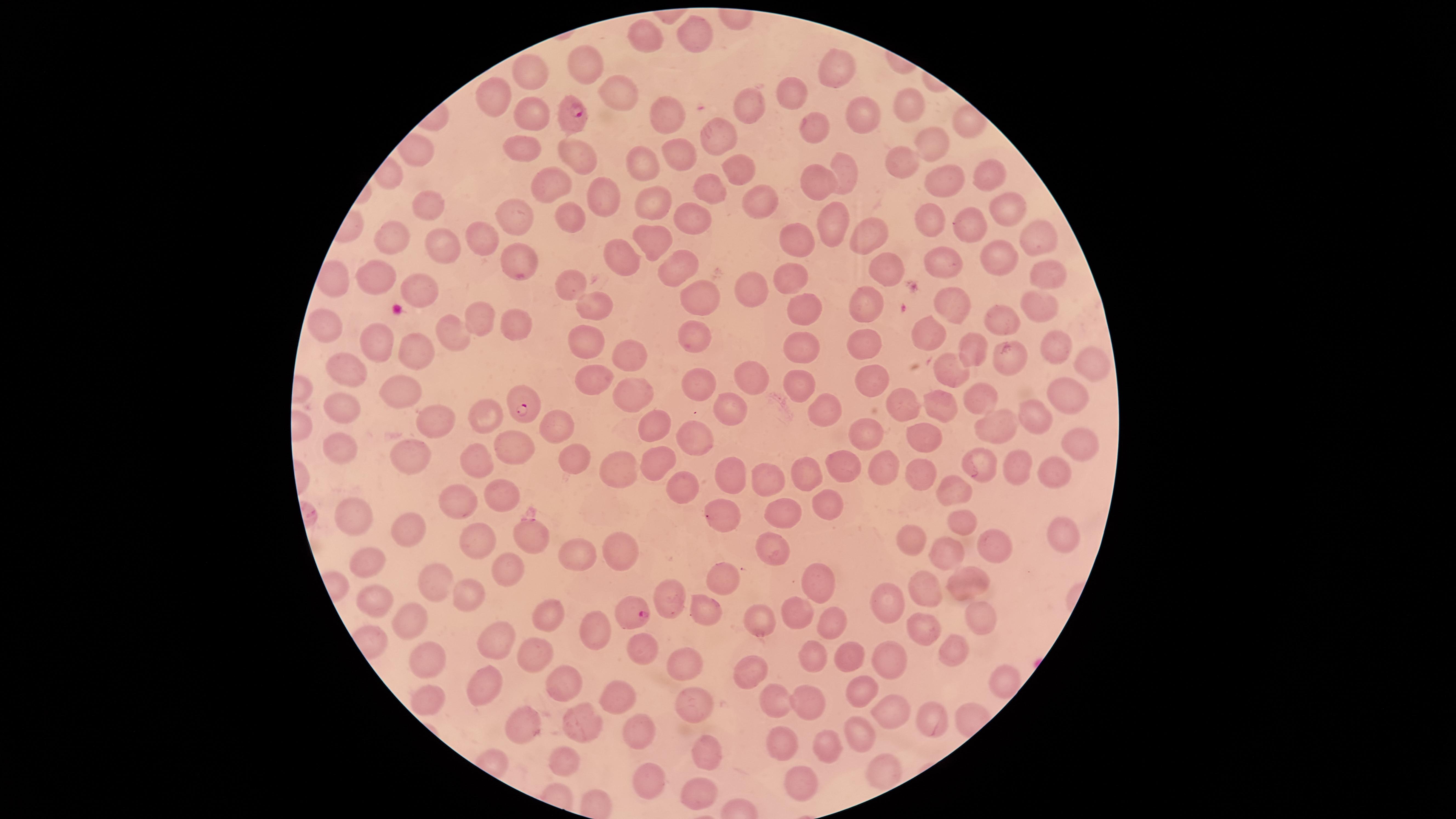

uninfected red blood cells = approximate marker points as [x, y] in pixels: [641, 31], [697, 36], [581, 67], [835, 67], [533, 76], [790, 90], [621, 91], [496, 95], [905, 99], [750, 105], [530, 114], [861, 116], [665, 118], [819, 125], [713, 136], [927, 136], [523, 143], [576, 148], [676, 158], [907, 162], [645, 165], [735, 167], [847, 172], [992, 175], [817, 182], [551, 183], [940, 185], [710, 187], [602, 198], [649, 200], [767, 200], [424, 206], [1010, 207], [515, 215], [570, 218], [687, 219], [930, 221], [828, 224], [975, 226], [1034, 229], [796, 233], [392, 234], [655, 237], [869, 237], [483, 240], [440, 244], [992, 253], [518, 255], [934, 257], [621, 258], [882, 265], [678, 267], [1047, 267], [374, 276], [793, 280], [565, 283], [420, 287], [756, 293], [698, 296], [953, 302], [589, 304], [1038, 304], [863, 307], [803, 308], [472, 313], [511, 318], [1004, 323], [324, 325], [445, 326], [691, 331], [930, 334], [581, 341], [865, 341], [969, 342], [368, 344], [1053, 345], [799, 348], [412, 351], [626, 354], [1011, 356], [1084, 359], [948, 362], [342, 370], [596, 377], [874, 377], [753, 379], [798, 380], [697, 384], [397, 392], [632, 394], [983, 395], [1063, 396], [935, 400], [823, 405], [341, 406], [731, 408], [1032, 410], [484, 416], [995, 420], [654, 421], [554, 422], [434, 424], [919, 433], [698, 434], [860, 434], [343, 442], [1077, 442], [523, 445], [413, 452], [572, 457], [470, 460], [1020, 464], [655, 465], [985, 465], [844, 466], [878, 466], [614, 468], [1058, 471], [808, 472], [728, 476], [769, 476], [914, 476], [680, 486], [500, 491], [951, 491], [457, 497], [822, 502], [783, 511], [355, 512], [722, 519], [968, 521], [410, 528], [1067, 533], [526, 536], [480, 540], [910, 542], [1001, 543], [613, 545], [770, 546], [566, 550], [940, 550], [362, 557], [508, 572], [721, 577], [963, 578], [428, 580], [817, 581], [931, 588], [466, 594], [372, 596], [668, 599], [888, 599], [705, 607], [798, 611], [973, 613], [549, 615], [409, 617], [760, 619], [833, 620], [597, 627], [926, 629], [499, 643], [644, 646], [954, 651], [853, 653], [530, 654], [430, 656], [814, 657], [889, 659], [683, 662], [1001, 669], [755, 674], [483, 679], [560, 679], [863, 688], [620, 697], [802, 697], [425, 700], [694, 701], [774, 701], [890, 710], [579, 724], [932, 725], [528, 727], [863, 733], [644, 737], [782, 740], [825, 747], [709, 749], [566, 758], [883, 770], [649, 776], [798, 781], [698, 794]
stain = Giemsa
preparation = thin blood smear
visible region = circular
field of view = single
species = Plasmodium falciparum
capture = smartphone photograph through the microscope eyepiece
presence = malaria parasites detected
parasitized red blood cells = approximate marker points as [x, y] in pixels: [572, 113], [521, 405], [633, 610]
image size = 1456×819 pixels